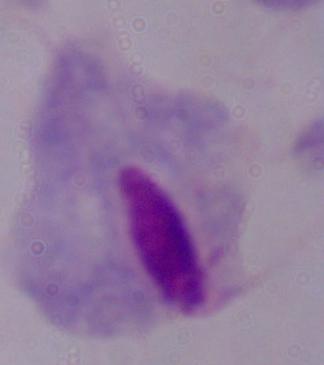
Summary:
  - Modality: photomicrograph
  - Identification: trichomonad
  - Magnification: 1000x